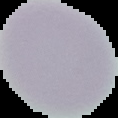

The area outside the segmented cell region is set to black. Image is 118×118 pixels. Malaria status: uninfected. From a thin blood film.